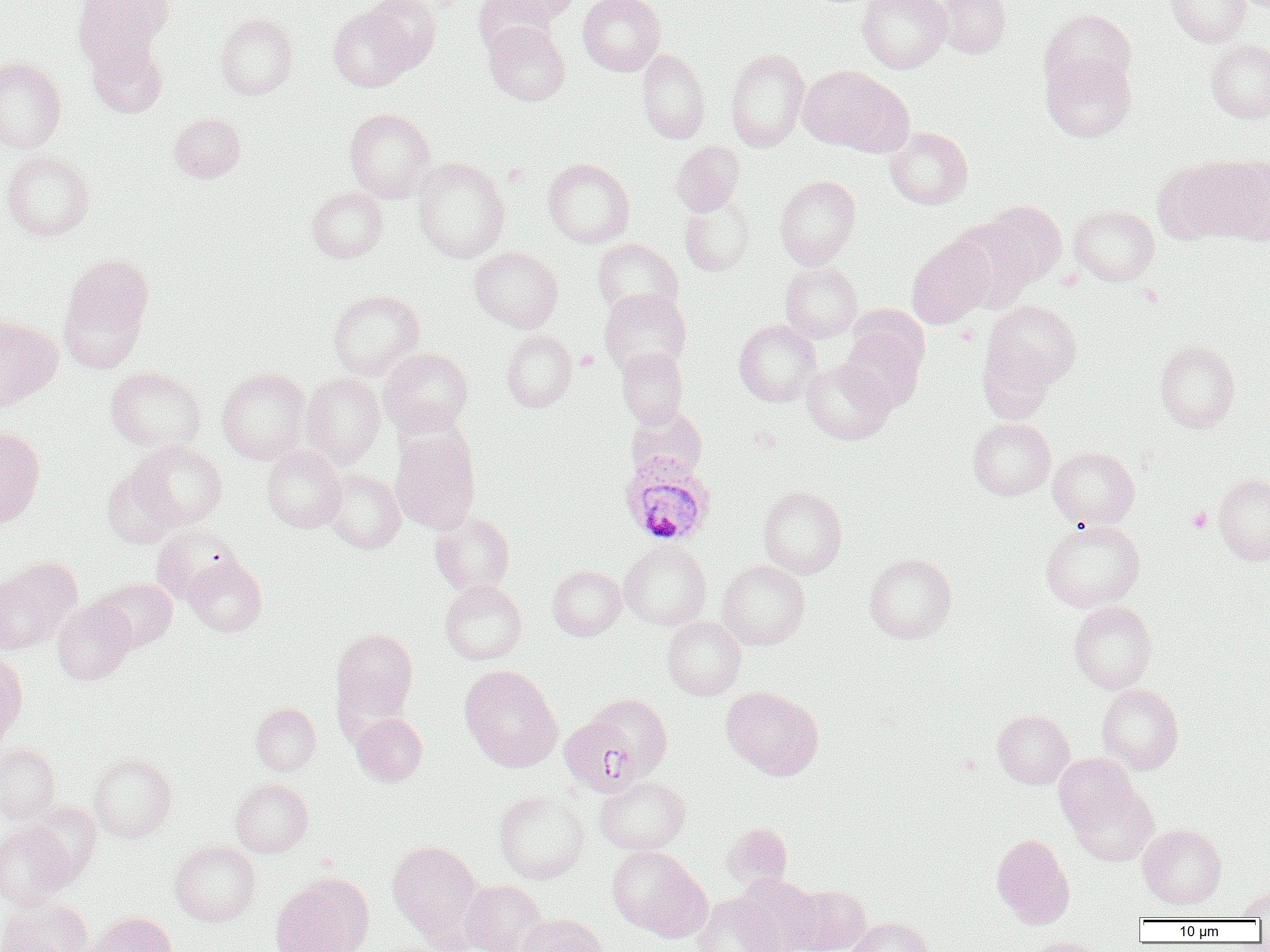
{
  "slide_level_diagnosis": "Plasmodium ovale",
  "magnification": "1000x",
  "image_size": "1270×952 pixels",
  "platelet_locations": "approximate bounding boxes as (x1,y1)-(x2,y2) corner pairs in pixels: (1188,508)-(1212,532)",
  "plasmodium_ovale_infected_red_blood_cell_locations": "approximate bounding boxes as (x1,y1)-(x2,y2) corner pairs in pixels: (620,453)-(716,546)",
  "field_of_view": "one of a larger specimen",
  "preparation": "thin blood film",
  "uninfected_red_blood_cell_locations": "approximate bounding boxes as (x1,y1)-(x2,y2) corner pairs in pixels: (73,0)-(171,71), (364,0)-(441,72), (474,0)-(558,54), (491,0)-(582,26), (578,0)-(665,75), (857,0)-(951,73), (935,0)-(1011,58), (1166,0)-(1252,46), (329,5)-(417,91), (1040,8)-(1137,94), (215,13)-(299,99), (483,22)-(570,106), (1206,38)-(1270,123), (87,39)-(168,119), (637,48)-(710,143), (725,48)-(809,151), (1041,52)-(1136,142), (0,57)-(66,153), (798,65)-(908,154), (344,108)-(436,202), (169,113)-(246,182), (886,127)-(973,209), (672,141)-(744,216), (2,151)-(94,240), (1213,155)-(1270,244), (412,157)-(509,262), (543,158)-(634,248), (1152,158)-(1257,243), (775,175)-(860,269), (307,187)-(388,262), (679,196)-(757,276), (979,200)-(1067,288), (1069,205)-(1159,286), (907,236)-(995,328), (592,238)-(683,319), (470,247)-(563,332), (58,255)-(154,372), (780,262)-(863,342), (599,288)-(691,376), (328,289)-(424,379), (982,301)-(1081,393), (0,315)-(62,408), (734,319)-(821,407), (839,327)-(926,413), (501,330)-(577,412), (1154,340)-(1240,431), (978,344)-(1059,422), (616,347)-(688,427), (379,348)-(473,436), (801,359)-(895,444), (106,367)-(206,452), (216,368)-(311,463), (302,373)-(385,468), (968,417)-(1056,500), (0,427)-(46,527), (390,429)-(480,533), (129,439)-(227,529), (262,446)-(346,532), (1048,446)-(1140,528), (102,466)-(180,548), (321,468)-(405,553), (1213,474)-(1270,564), (757,486)-(847,579), (430,512)-(515,595), (1040,519)-(1144,611), (151,525)-(243,603), (619,542)-(711,630), (864,552)-(956,643), (184,557)-(267,637), (0,558)-(82,652), (717,560)-(810,649), (548,566)-(626,640), (90,577)-(177,650), (440,580)-(528,664), (52,598)-(136,684), (1069,601)-(1156,694), (662,616)-(746,700), (330,628)-(419,725), (0,654)-(28,742), (460,665)-(562,772), (1097,684)-(1184,774), (721,686)-(823,779), (585,692)-(673,779), (251,703)-(321,774), (992,709)-(1075,788), (352,713)-(427,786), (0,742)-(61,822), (88,753)-(177,841), (1053,753)-(1137,833), (595,776)-(690,855), (231,778)-(313,857), (1069,784)-(1158,866), (494,790)-(589,883), (25,801)-(102,883), (722,822)-(792,891), (1138,824)-(1226,908), (0,825)-(71,906), (991,833)-(1075,928), (170,840)-(260,925), (387,840)-(485,941), (607,845)-(710,940), (735,873)-(823,952), (270,874)-(374,952), (460,880)-(547,952), (787,883)-(871,952), (1234,887)-(1270,919), (692,893)-(782,952), (1,898)-(92,952), (86,911)-(177,951), (518,913)-(609,952), (846,917)-(934,952), (1027,936)-(1106,952)",
  "modality": "optical microscopy"
}